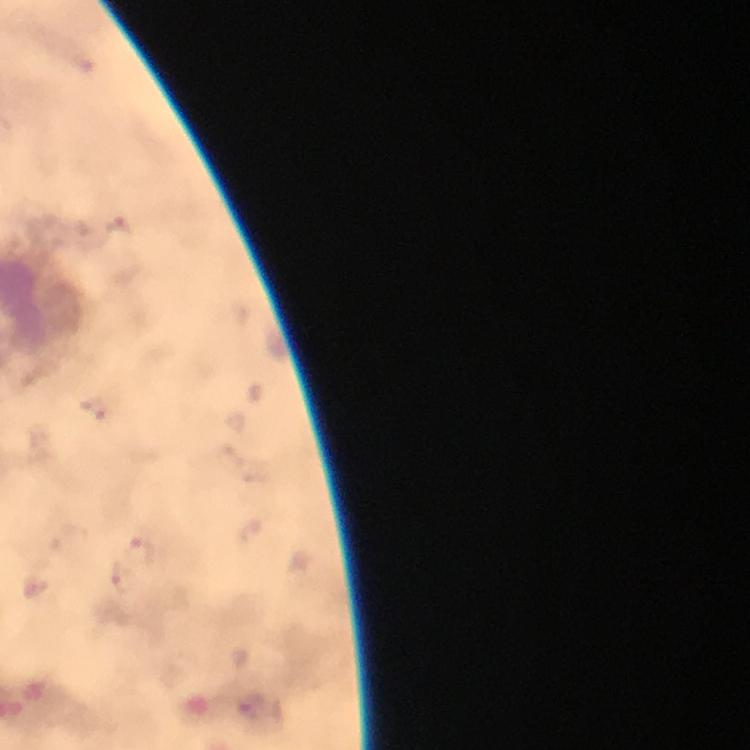

Approximate object centers, in pixels from the top-left corner.
Summary:
  - Plasmodium parasite locations: (x=118, y=225), (x=95, y=410), (x=140, y=550), (x=128, y=580)
  - Cropped from: one field of view
  - Immersion oil: used
  - Preparation: thick blood smear
  - Capture: smartphone mounted on the microscope
  - Image size: 750×750 pixels
  - Context: from a malaria diagnostic workup
  - Magnification: 100x
  - Stain: Giemsa